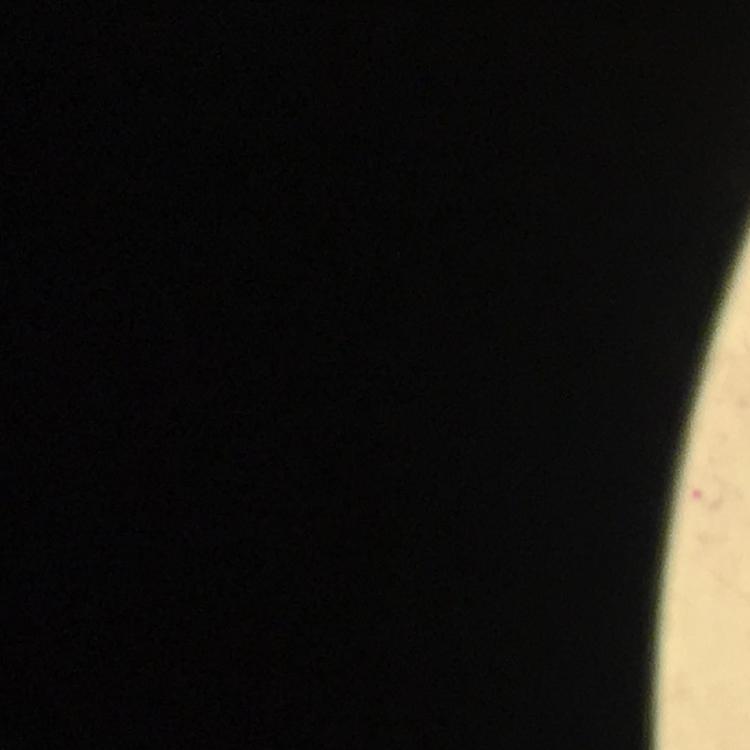

Approximate object centers, in pixels from the top-left corner.
Summary:
  - Plasmodium parasite locations: (x=710, y=497)
  - Cropped from: a single field of view
  - Magnification: 100x
  - Capture: smartphone photograph through a microscope
  - Stain: Giemsa
  - Image size: 750×750 pixels
  - Preparation: thick smear
  - Context: from a diagnostic examination for malaria
  - Immersion oil: used